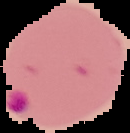

Result: malaria parasites identified. From a thin blood film. Image is 130×133 pixels. Segmented cell region on a black background.